Identify the cell.
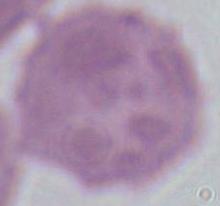
This is an erythrocyte.

1000x magnification. Micrograph.